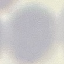
malaria status = uninfected
image type = cell patch, automatically extracted from a larger field of view and resized to 64 × 64 pixels
preparation = thin blood smear
capture = smartphone camera at the microscope eyepiece
stain = Giemsa